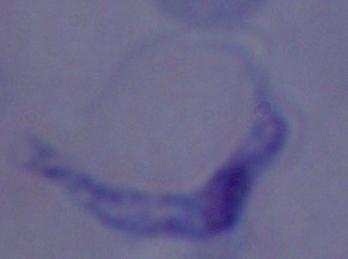

modality: photomicrograph
identification: trypanosome
magnification: 1000x